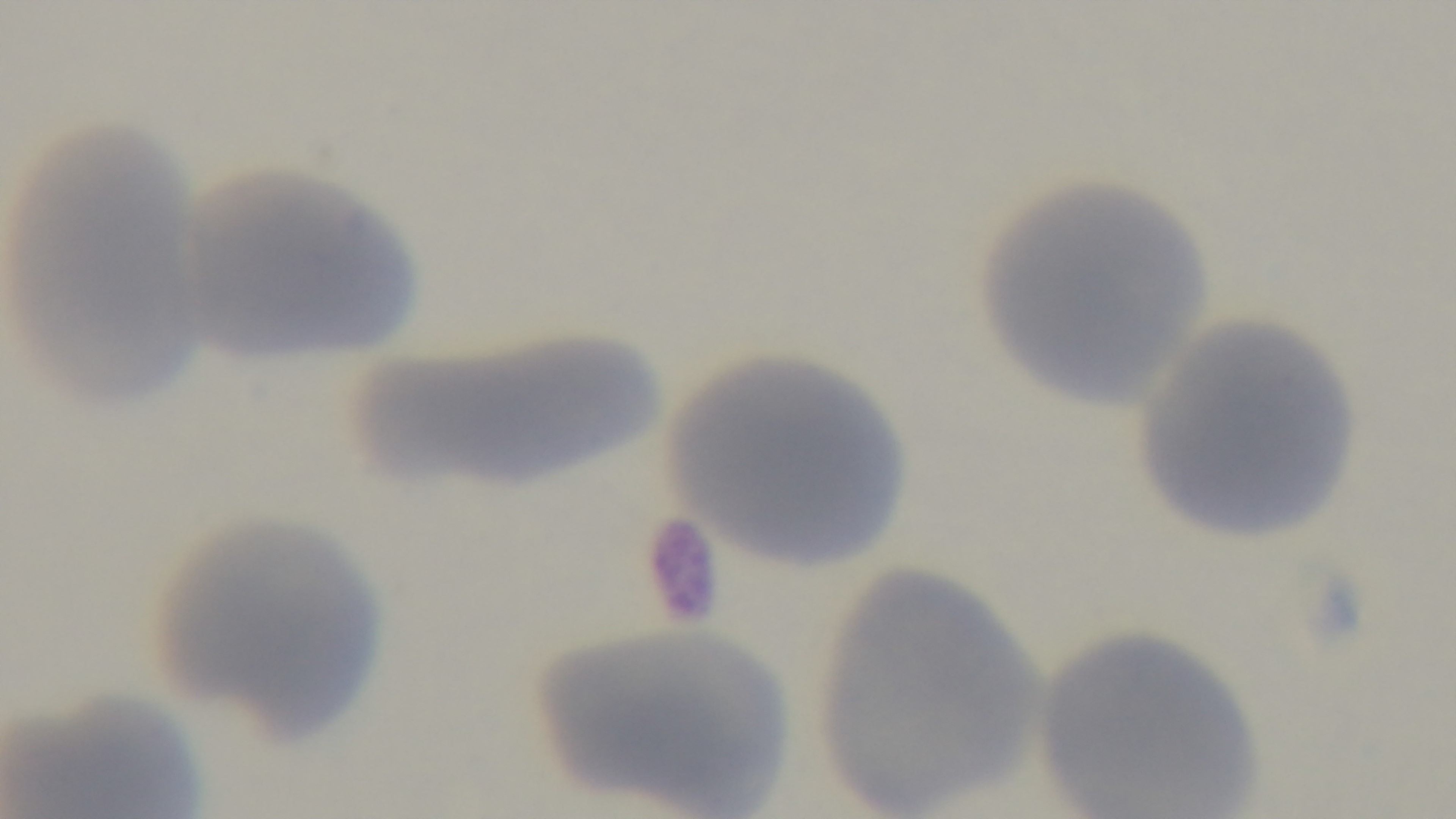
Single field of view. Preparation: thin. Malaria status: negative. Giemsa stain. 100x oil-immersion objective. Captured with a mounted 4K digital camera. Photomicrograph.